Give the position of each P. falciparum parasite with its life-cycle stage, each leukocyte, and any debris.
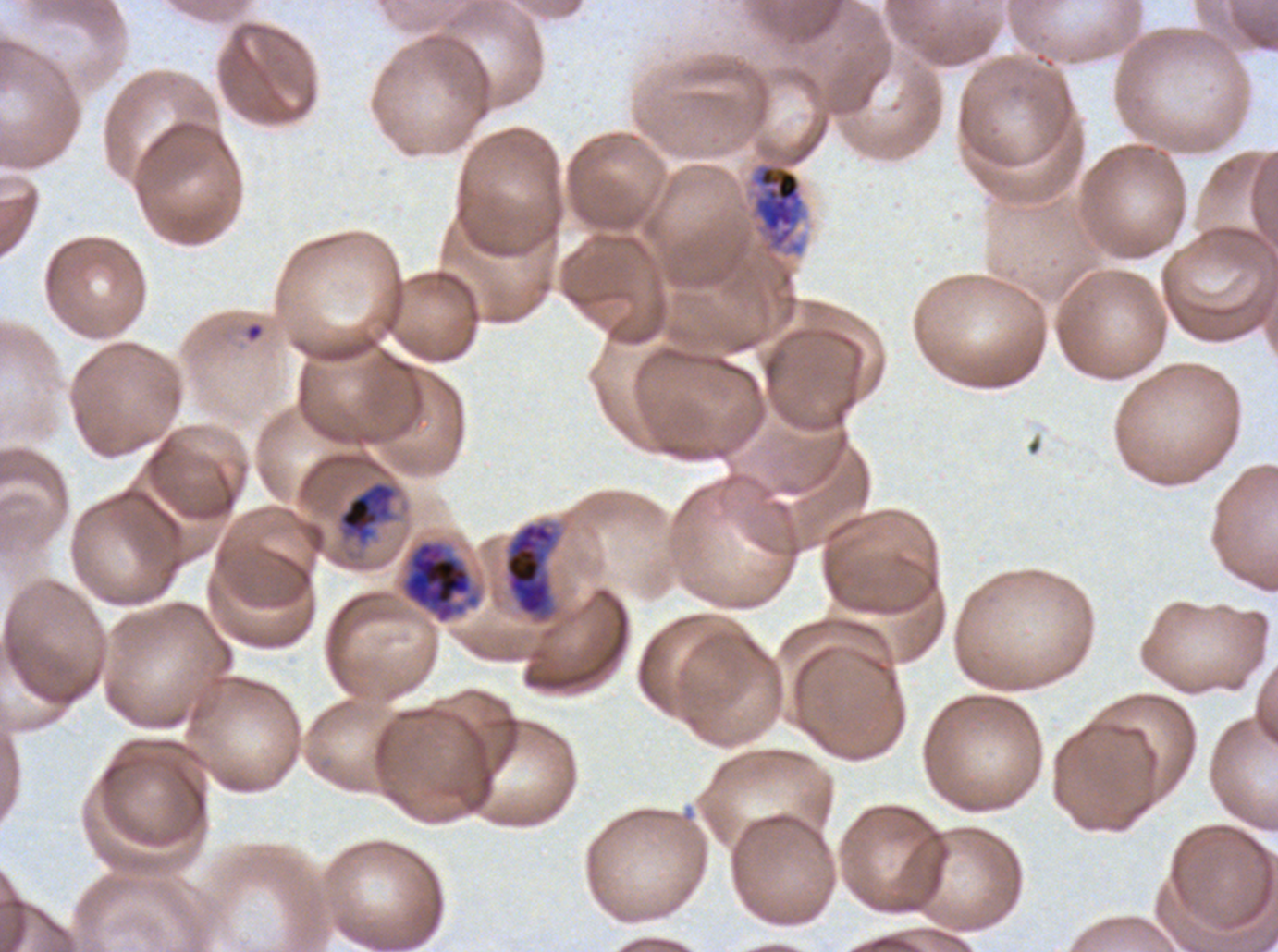
Approximate bounding boxes as (x1, y1, x2, y2) in pixels.
Rings: (244, 322, 264, 343).
Late trophozoites: (339, 482, 395, 538).
Early schizonts: (747, 162, 806, 256), (504, 521, 558, 621).
Late schizonts: (400, 540, 481, 624).
No late-ring/early-trophozoite forms, mid trophozoites, segmenters, gametocytes, leukocytes, or debris observed.

Summary:
  - Field of view: sub-image separated from a larger composite
  - Life-cycle stages observed: ring, late trophozoite, early schizont, late schizont
  - Preparation: thin blood film
  - Image size: 1278×952 pixels
  - Specimen: P. falciparum from a patient in The Gambia, cultured ex vivo for 24 to 48 hours
  - Stain: Giemsa